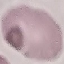
result = no malaria parasites seen
capture = smartphone through the microscope eyepiece
preparation = thin blood film
image type = automatically extracted cell patch, resized to 64 × 64 pixels
stain = Giemsa